Report the malaria status of this cell.
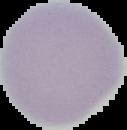
It is uninfected.

Summary:
  - Image size: 127×130 pixels
  - Image type: segmented cell region with the area outside set to black
  - Preparation: thin blood smear